Name the cell type shown.
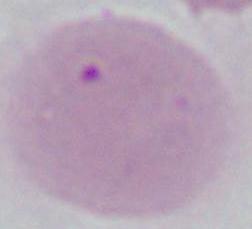

An erythrocyte.

Captured at 1000x magnification. Photomicrograph.